Classify this cell by malaria status.
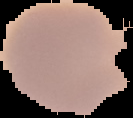

Uninfected.

preparation: thin blood film
image_type: cell region segmented out of the field of view; surrounding area masked to black
image_size: 133×118 pixels